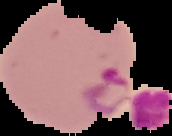

{
  "image_type": "segmented cell region with the area outside set to black",
  "preparation": "thin blood smear",
  "image_size": "172×136 pixels",
  "malaria_status": "parasitized"
}